Assess the morphology of the erythrocytes.
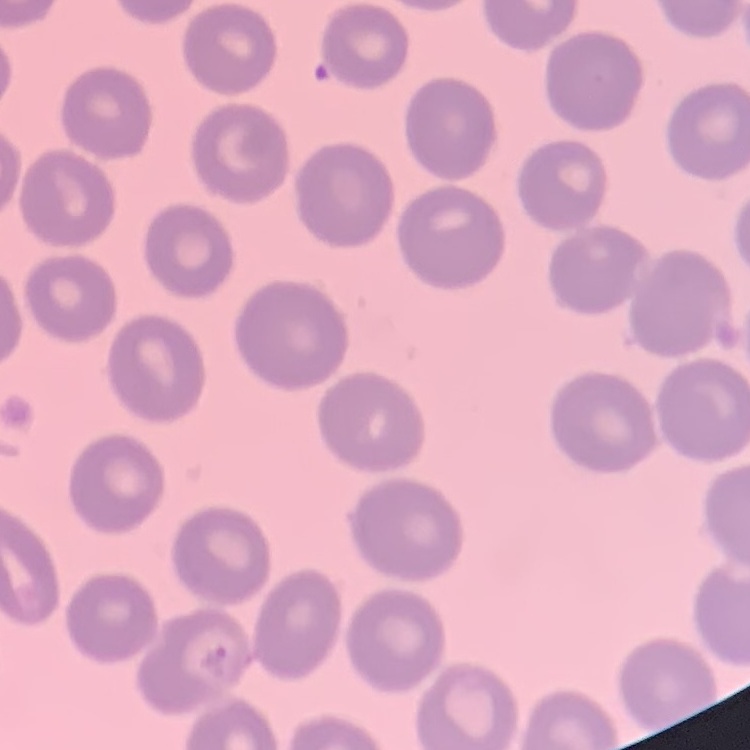

No rouleaux formation.

Summary:
  - Stain: Field's or Giemsa
  - Image type: square crop of a larger photomicrograph
  - Preparation: thin blood smear